Give the position of every malaria parasite.
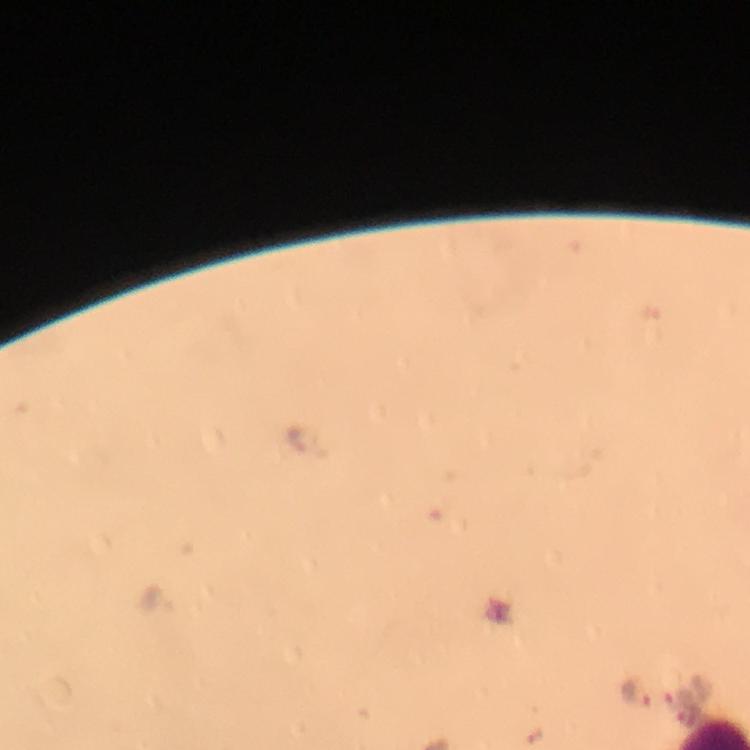
Approximate object centers, in pixels from the top-left corner.
Malaria parasites: (x=296, y=438), (x=635, y=693), (x=686, y=715).

Summary:
  - Image size: 750×750 pixels
  - Stain: Giemsa
  - Cropped from: one field of view
  - Immersion oil: applied
  - Preparation: thick blood film
  - Capture: smartphone photograph through a microscope
  - Context: from a malaria diagnostic workup
  - Magnification: 100x